Classify this cell by malaria status.
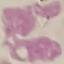
Uninfected.

Summary:
  - Stain: Giemsa
  - Capture: smartphone camera at the microscope eyepiece
  - Preparation: thin blood film
  - Image type: automatically extracted cell patch, resized to 64 × 64 pixels